Classify this cell by malaria status.
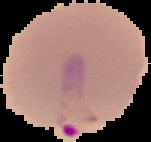

It is parasitized.

From a thin blood film. The area outside the segmented cell region is set to black. Image is 151×142 pixels.